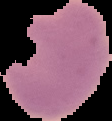

Summary:
  - Image size: 112×121 pixels
  - Result: no Plasmodium parasites seen
  - Preparation: thin blood film
  - Image type: cell region segmented out of the field of view; surrounding area masked to black